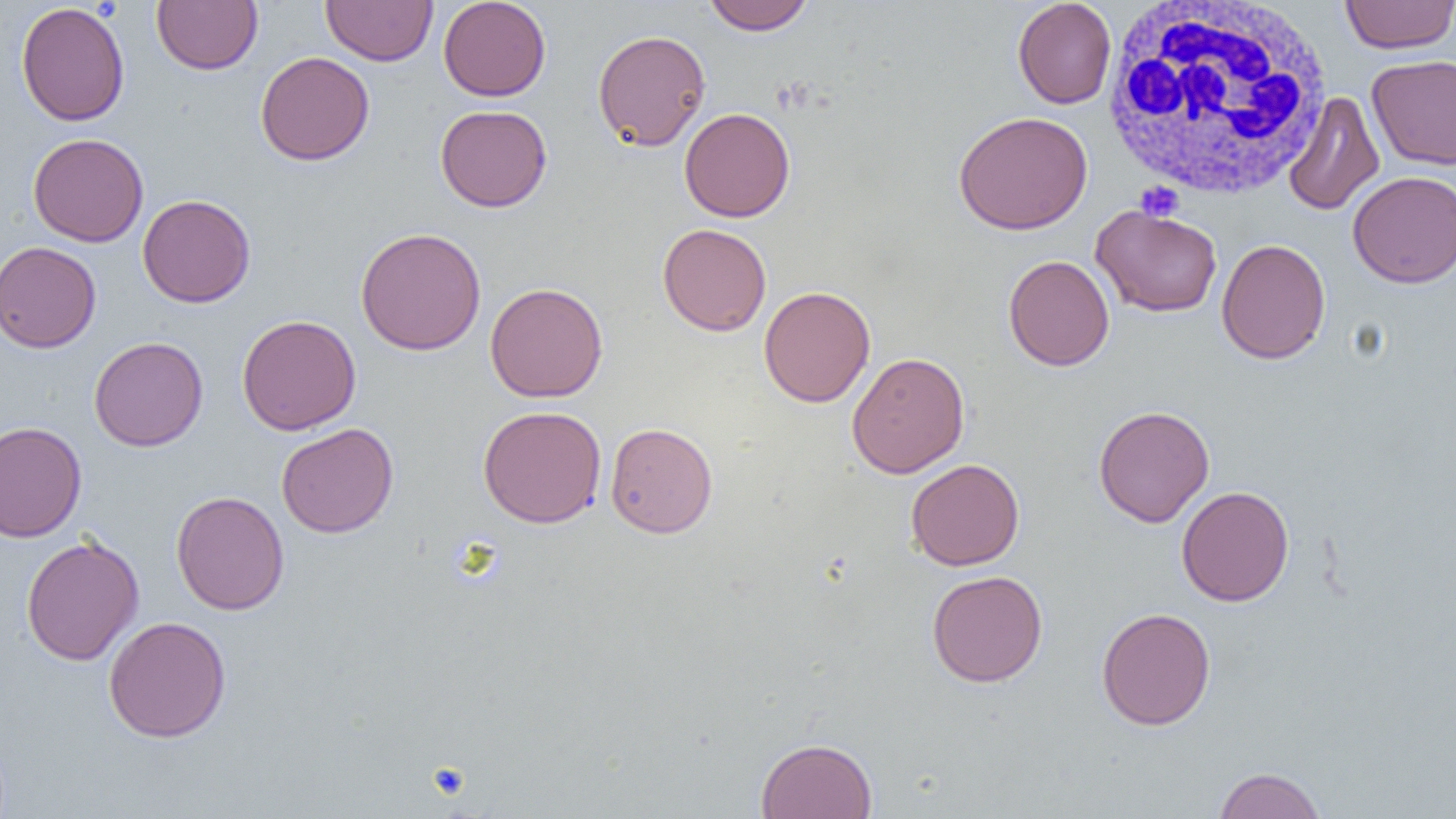
slide-level diagnosis = no evidence of blood parasites
uninfected red blood cell locations = approximate bounding boxes as [x1, y1, x2, y2] in pixels: [151, 0, 262, 75], [321, 0, 438, 66], [438, 0, 551, 102], [703, 0, 815, 35], [1012, 0, 1117, 109], [1340, 0, 1455, 53], [16, 1, 130, 126], [593, 29, 711, 151], [255, 51, 375, 165], [1366, 54, 1456, 170], [1283, 91, 1385, 216], [435, 104, 552, 212], [679, 107, 795, 222], [953, 111, 1093, 235], [28, 133, 149, 247], [1347, 170, 1456, 288], [138, 194, 255, 308], [1091, 205, 1222, 317], [657, 223, 772, 336], [356, 226, 487, 356], [1216, 237, 1331, 364], [0, 241, 102, 353], [1003, 255, 1114, 371], [485, 282, 608, 402], [759, 285, 876, 408], [236, 314, 361, 435], [89, 336, 208, 451], [846, 351, 970, 478], [1093, 404, 1215, 527], [478, 405, 606, 528], [0, 420, 87, 543], [605, 422, 718, 538], [276, 423, 398, 538], [905, 458, 1025, 571], [1176, 485, 1294, 607], [171, 491, 290, 615], [20, 534, 144, 666], [926, 570, 1048, 687], [1096, 606, 1216, 730], [103, 616, 232, 742], [755, 737, 878, 818], [1213, 766, 1328, 819]
image size = 1456×819 pixels
white blood cell locations = approximate bounding boxes as [x1, y1, x2, y2] in pixels: [1100, 0, 1334, 201]
modality = optical microscopy
field of view = single
preparation = thin blood film
magnification = 1000x
platelet locations = approximate bounding boxes as [x1, y1, x2, y2] in pixels: [1135, 181, 1184, 222], [427, 762, 471, 802]